State which parasite is depicted.
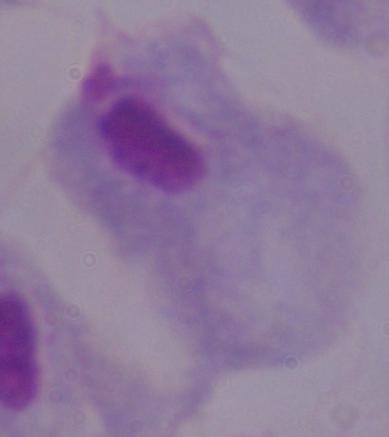

A trichomonad.

Photomicrograph. 1000x magnification.